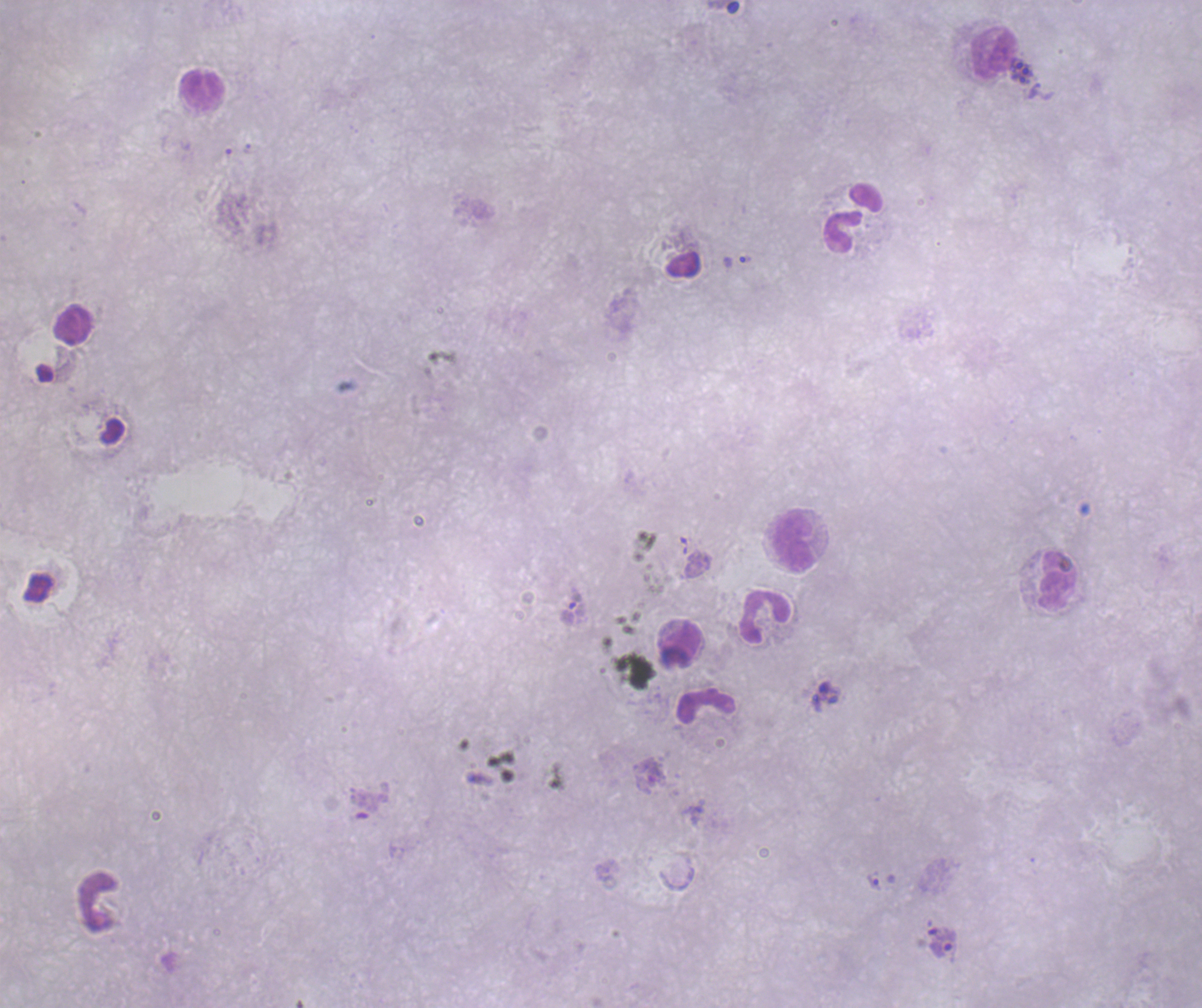
Approximate centers as (x, y) in pixels. Trophozoite locations: (745, 260), (875, 881), (942, 948). Leukocyte locations: (993, 52), (202, 89), (853, 219), (72, 325), (794, 541), (1059, 582), (765, 617), (682, 641), (706, 706). Schizont locations: (1024, 73). Life-cycle stages observed: trophozoite, schizont. Result: malaria parasites identified. Single field of view. Image is 1202×1008 pixels. Romanowsky-stained preparation. Previously used in an actual diagnosis. Background quality: unsatisfactory. Coloration quality: bad. 100x magnification. Thick blood film.